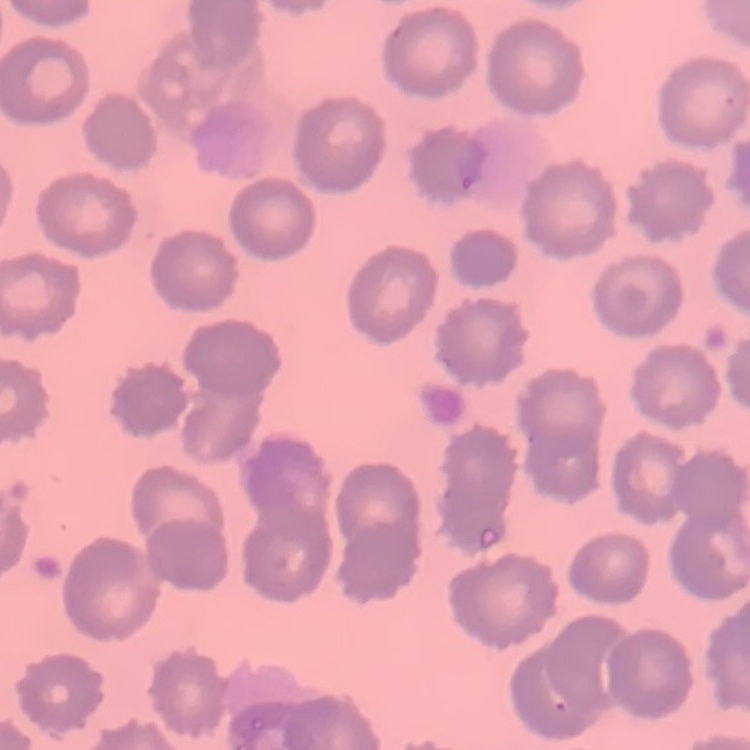
The erythrocytes show no rouleaux formation. Stained with either Field's or Giemsa. Thin blood smear. One tile cut from a larger photomicrograph.